Identify the parasite.
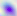
Toxoplasma gondii.

400x magnification. Photomicrograph.